Comment on the morphology of the erythrocytes.
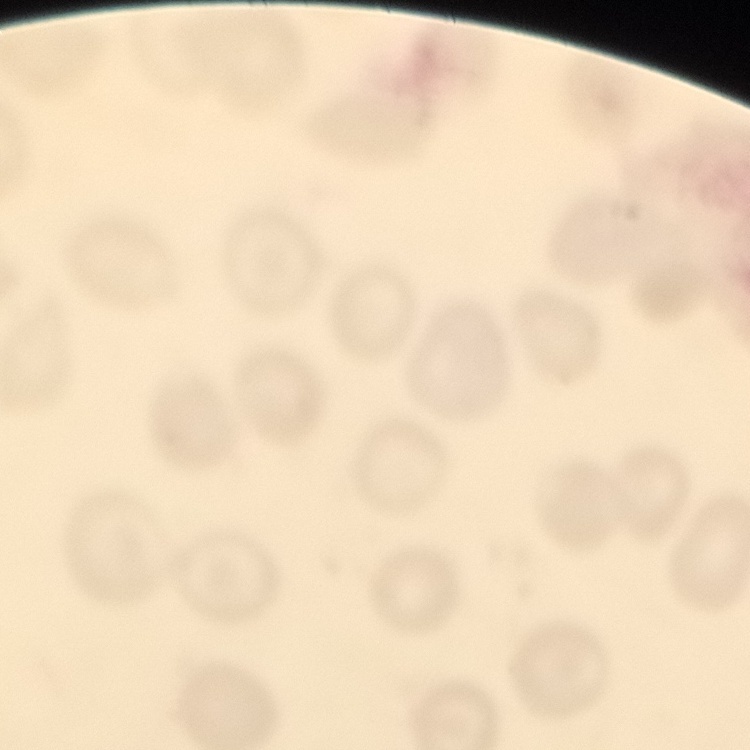

No rouleaux formation.

Field's or Giemsa stain. Thin blood smear. Square crop of a larger photomicrograph.